Assess this cell for malaria.
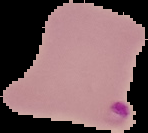
Parasitized.

Summary:
  - Image type: segmented cell region on a black background
  - Image size: 148×133 pixels
  - Preparation: thin blood smear